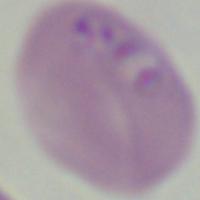
1000x magnification. Photomicrograph. A Babesia parasite is seen.